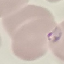

Malaria status: parasitized. Thin smear of blood. Acquired by smartphone through the microscope eyepiece. Automatically extracted cell patch, resized to 64 × 64 pixels. Giemsa stain.